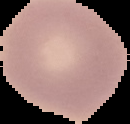

Summary:
  - Image type: segmented cell region on a black background
  - Result: no Plasmodium parasites detected
  - Image size: 130×124 pixels
  - Preparation: thin blood film